Assess this cell for malaria.
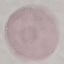
Uninfected.

Summary:
  - Image type: automatically extracted cell patch, resized to 64 × 64 pixels
  - Stain: Giemsa
  - Preparation: thin smear
  - Capture: smartphone through the microscope eyepiece